Assess for malaria.
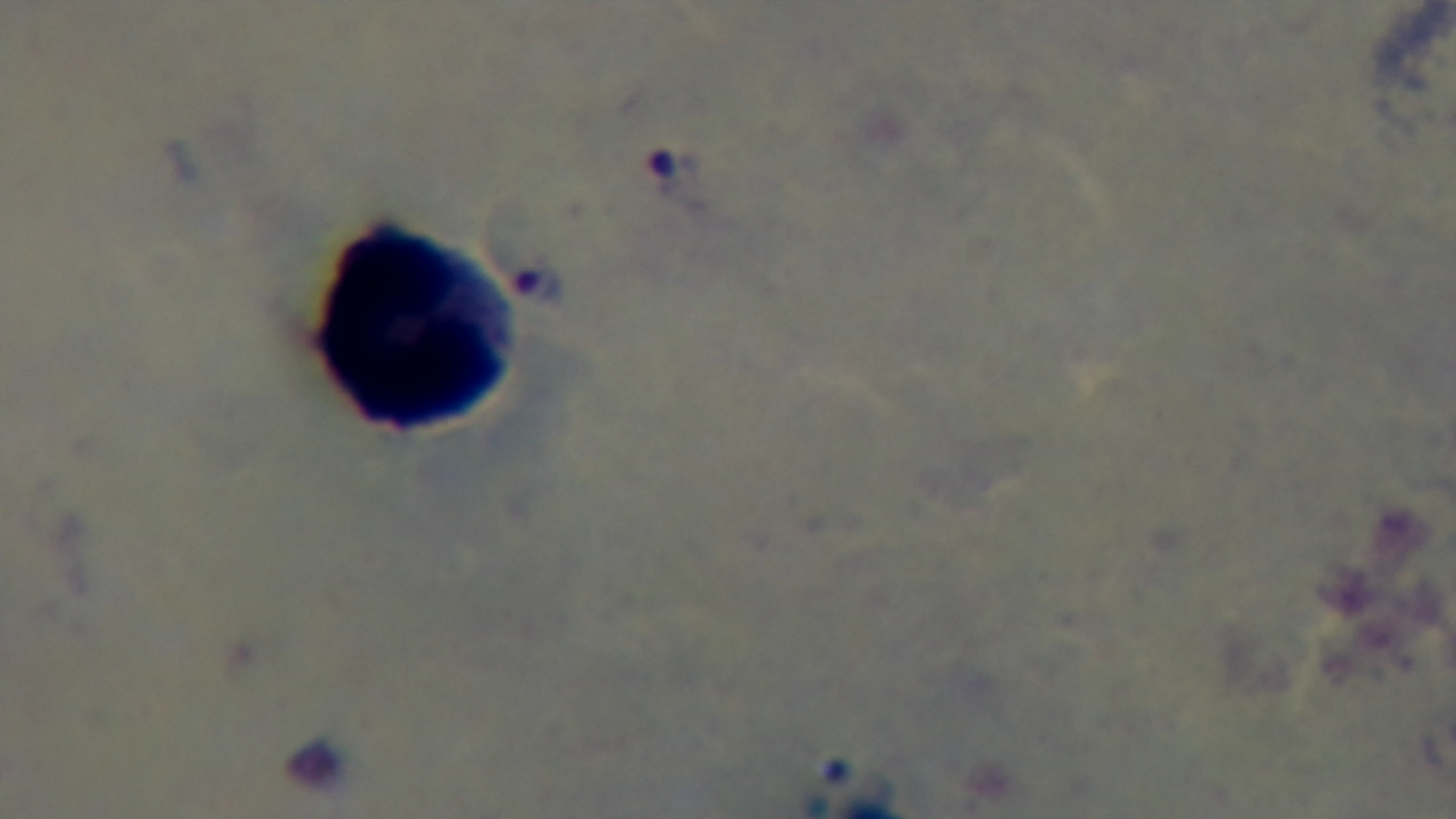
It is infected.

Summary:
  - Modality: light microscopy
  - Objective: 100x oil immersion
  - Preparation: thick
  - Capture: mounted 4K digital camera
  - Field of view: one from the slide
  - Stain: Giemsa